State which cell type is depicted.
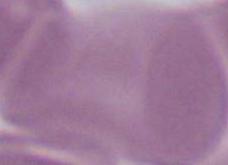
An erythrocyte.

Summary:
  - Modality: micrograph
  - Magnification: 1000x